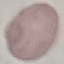
malaria status = uninfected
stain = Giemsa
capture = smartphone camera at the microscope eyepiece
image type = automatically extracted cell patch, resized to 64 × 64 pixels
preparation = thin blood film